State which parasite is depicted.
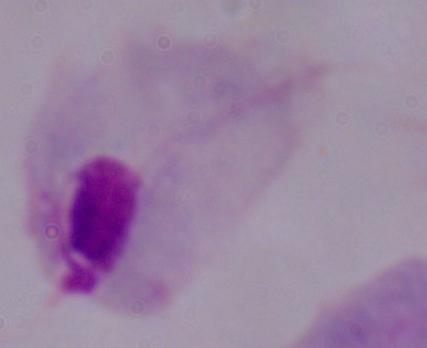

A trichomonad.

modality = photomicrograph
magnification = 1000x